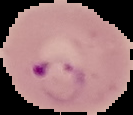
Cell region segmented out of the field of view; the surrounding area is masked to black. Image is 133×115 pixels. Malaria status: parasitized. From a thin blood smear.